Identify the preparation type.
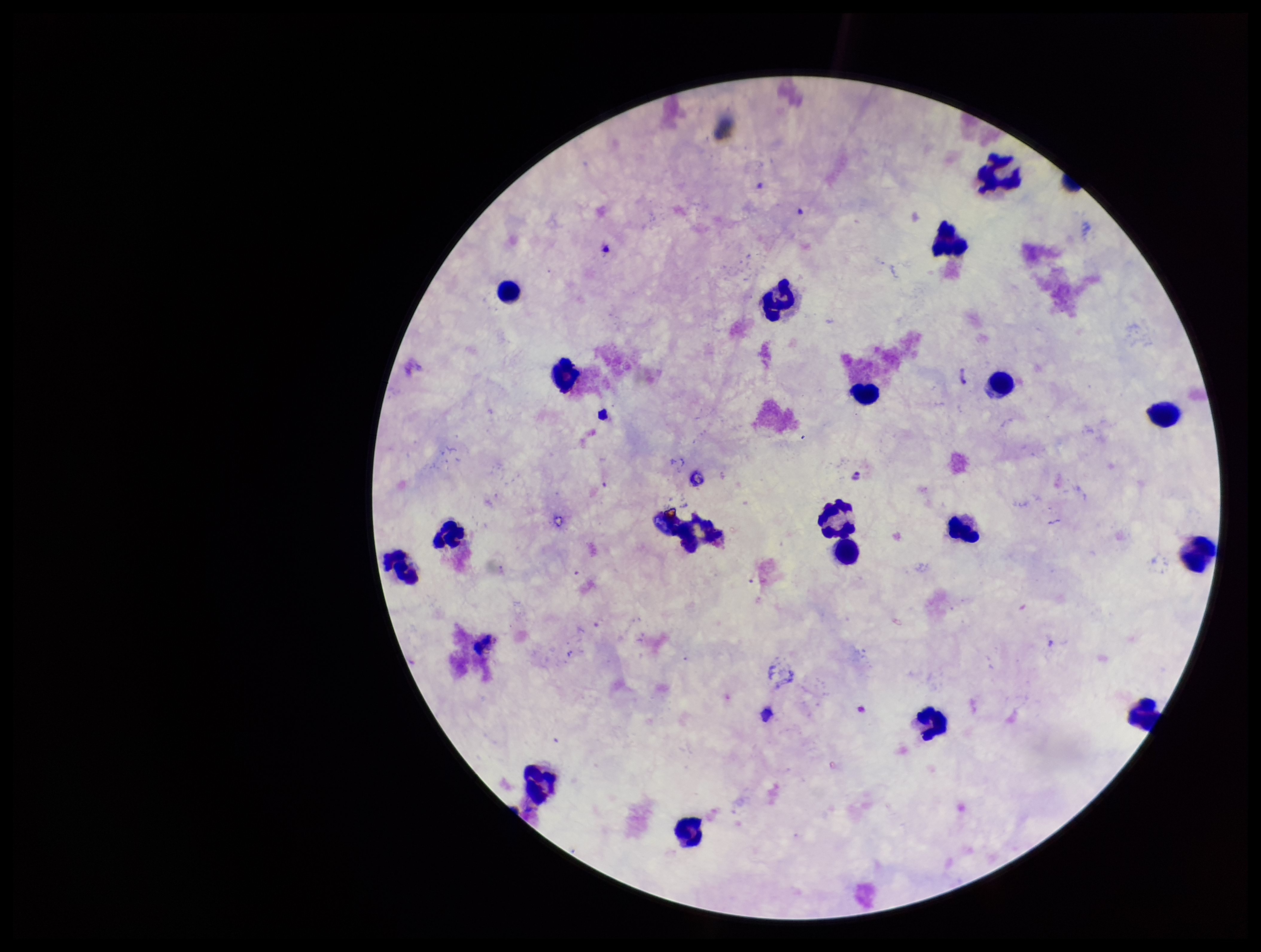

A thick smear.

Leukocyte count: 19. Stained with Giemsa. Patient malaria status: negative. One field from this slide. Photographed through the microscope eyepiece with a smartphone camera. Plasmodium parasites: none seen. Image is 1261×952 pixels. Parasite count: 0.